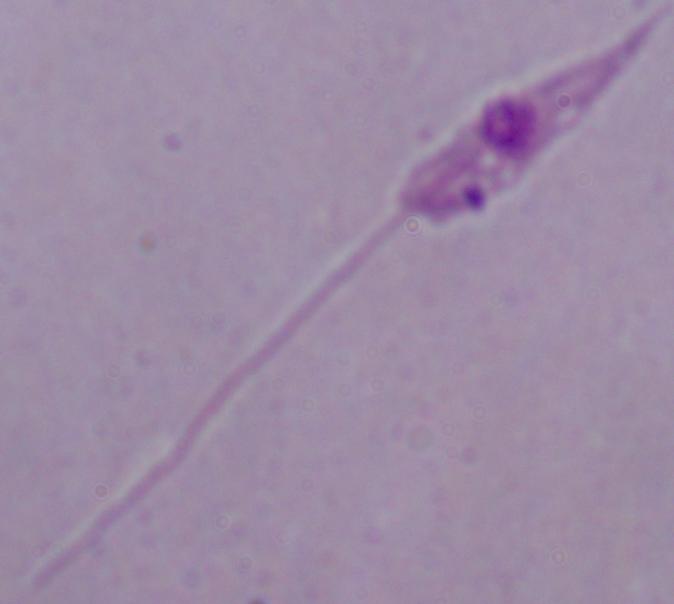

Summary:
  - Identification: Leishmania
  - Magnification: 1000x
  - Modality: photomicrograph